Give the preparation type.
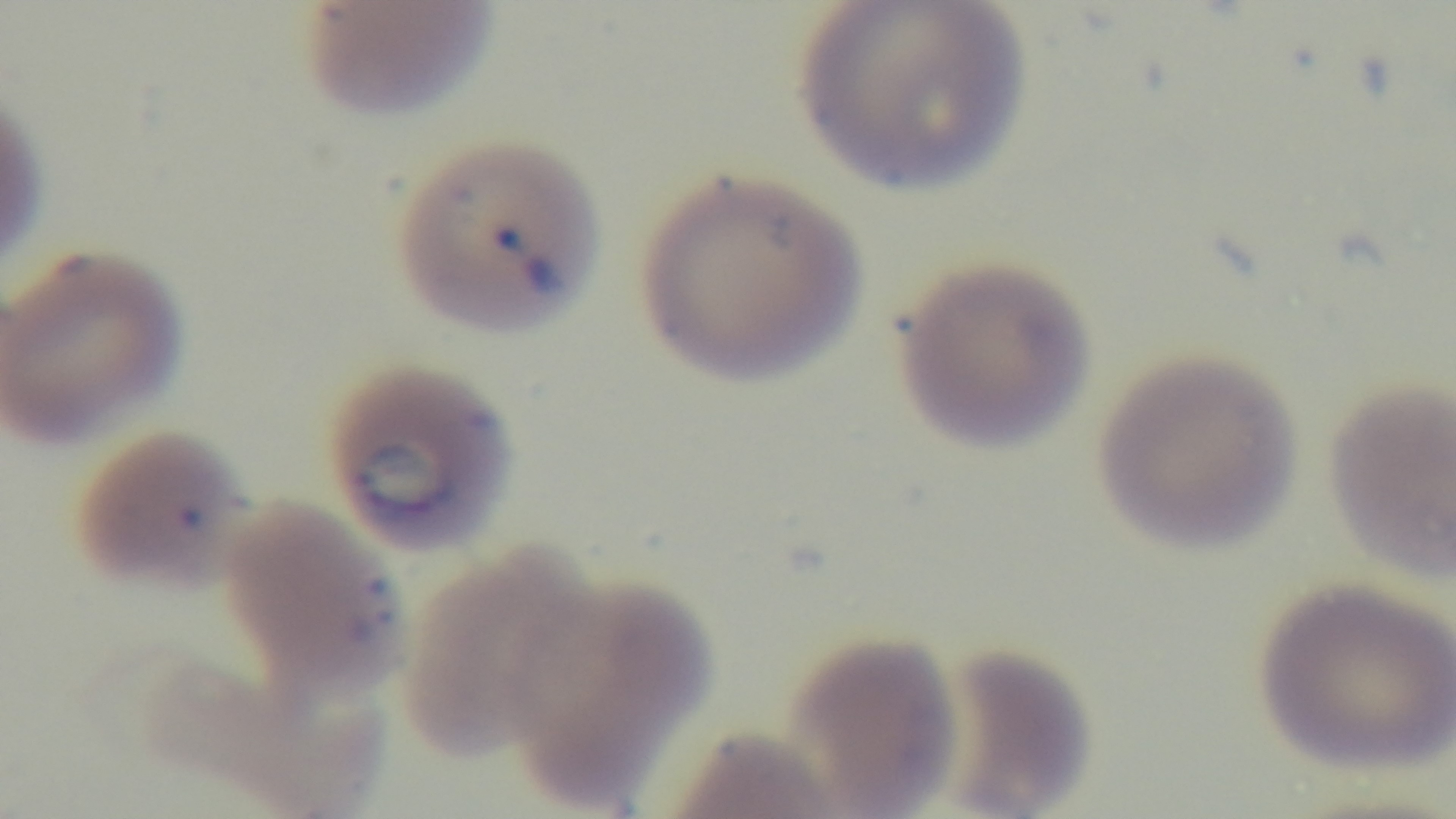

It is a thin blood film.

Summary:
  - Capture: mounted 4K digital camera
  - Field of view: one from the slide
  - Modality: light microscopy
  - Stain: Giemsa
  - Malaria status: positive
  - Objective: 100x oil immersion